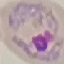
Malaria status: parasitized. Thin blood film. Giemsa stain. Acquired by smartphone through the microscope eyepiece. Cell patch, automatically extracted from a larger field of view and resized to 64 × 64 pixels.